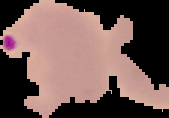 From a thin blood film. The area outside the segmented cell region is set to black. Result: malaria parasites detected. Image is 169×118 pixels.